Classify this cell by malaria status.
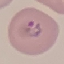

It is parasitized.

Summary:
  - Image type: cell patch, automatically extracted from a larger field of view and resized to 64 × 64 pixels
  - Capture: smartphone camera at the microscope eyepiece
  - Stain: Giemsa
  - Preparation: thin blood film